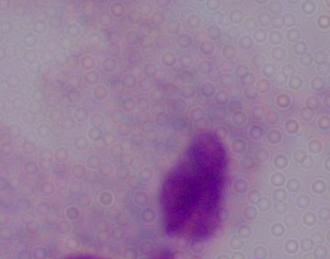
Summary:
  - Modality: micrograph
  - Identification: trichomonad
  - Magnification: 1000x